Assess this cell for malaria.
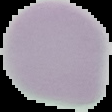

Uninfected.

Summary:
  - Image size: 112×112 pixels
  - Preparation: thin blood smear
  - Image type: cell region segmented out of the field of view; surrounding area masked to black